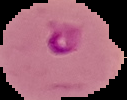 Segmented cell region on a black background. Image is 127×100 pixels. Result: malaria parasites identified. From a thin blood smear.